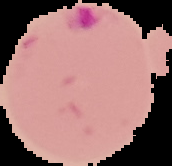 From a thin blood smear. The area outside the segmented cell region is set to black. Malaria status: parasitized. Image is 172×166 pixels.